Identify the parasite.
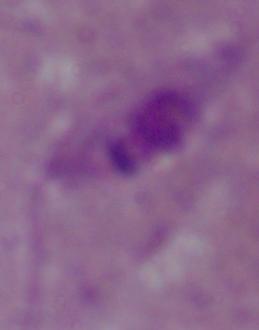
Leishmania.

Summary:
  - Modality: photomicrograph
  - Magnification: 1000x